Assess for malaria.
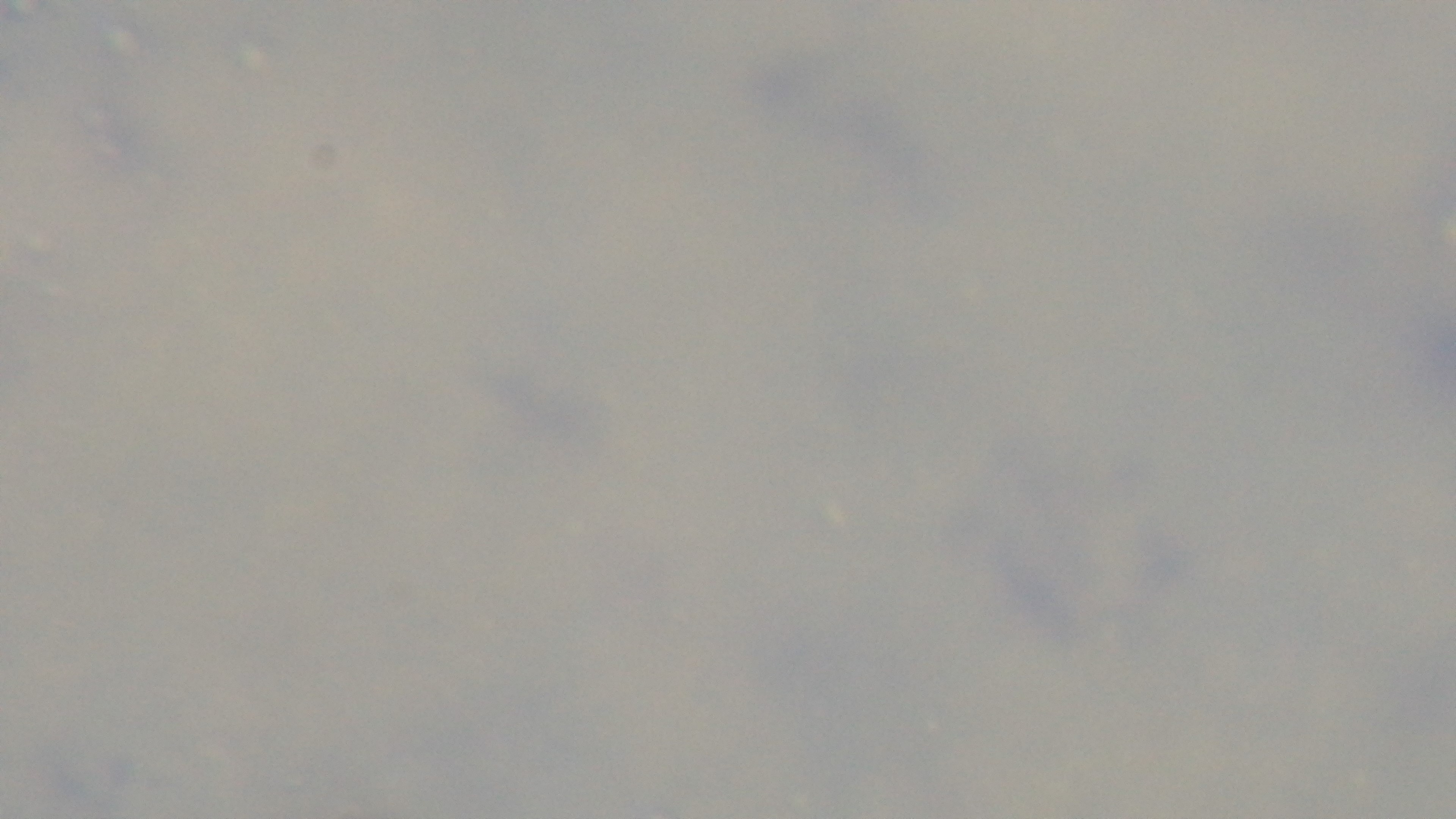

Uninfected.

Summary:
  - Objective: 100x oil immersion
  - Stain: Giemsa
  - Capture: mounted 4K digital camera
  - Modality: light microscopy
  - Field of view: single
  - Preparation: thick